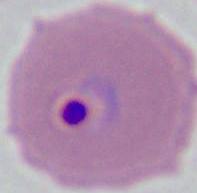
modality = micrograph
identification = Plasmodium
magnification = 400x or 1000x